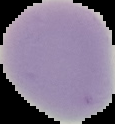

preparation = thin blood smear
result = no Plasmodium parasites detected
image size = 115×124 pixels
image type = segmented cell region with the area outside set to black